Assess the morphology of the erythrocytes.
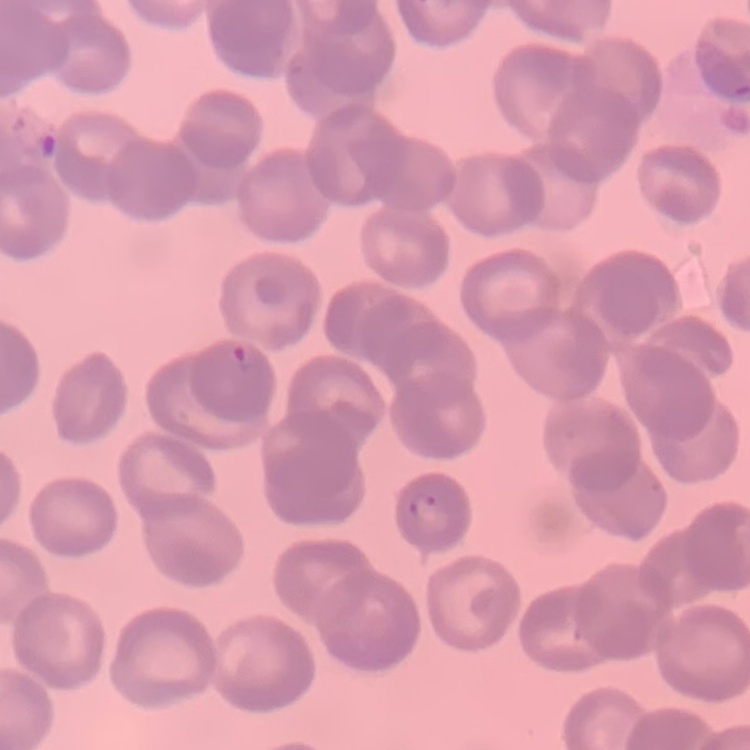

They show rouleaux formation.

{
  "stain": "Field's or Giemsa",
  "preparation": "thin blood film",
  "image_type": "one tile cut from a larger photomicrograph"
}